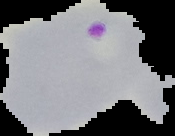

malaria status = parasitized
image size = 175×136 pixels
preparation = thin blood smear
image type = cell region segmented out of the field of view; surrounding area masked to black